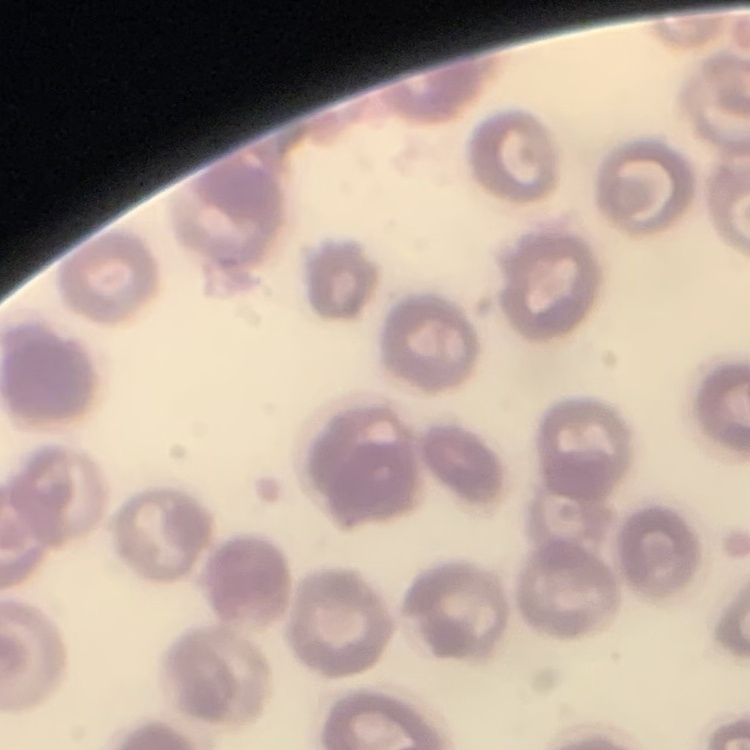
red blood cell morphology = no rouleaux formation
stain = Field's or Giemsa
image type = square crop of a larger photomicrograph
preparation = thin peripheral smear